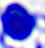

Micrograph. A leukocyte is seen. Captured at 400x magnification.